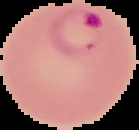

preparation: thin blood film
result: Plasmodium parasites identified
image_size: 139×130 pixels
image_type: segmented cell region with the area outside set to black